Describe the morphology of the erythrocytes.
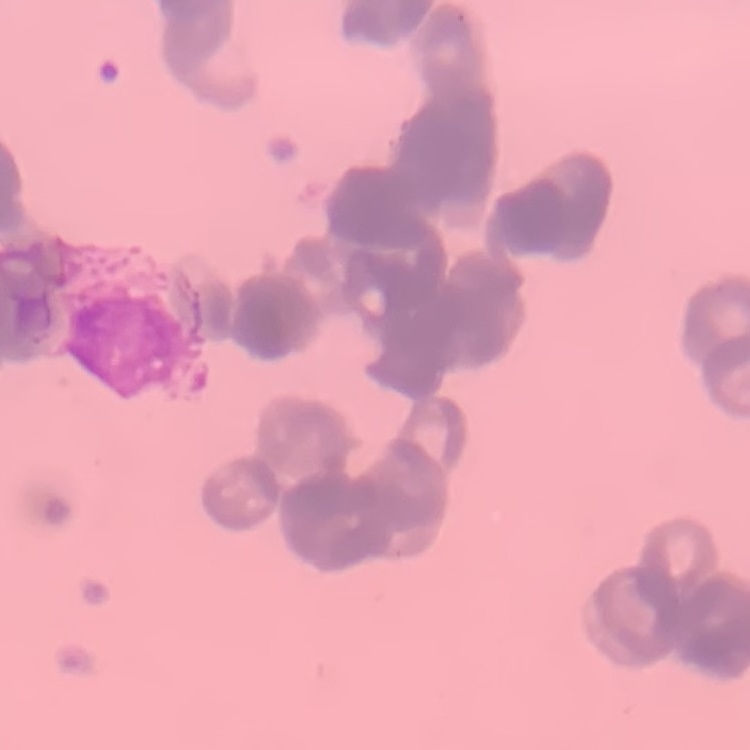

They show rouleaux formation.

Thin peripheral smear. Square crop of a larger photomicrograph. Field's or Giemsa stain.